Assess the morphology of the red blood cells.
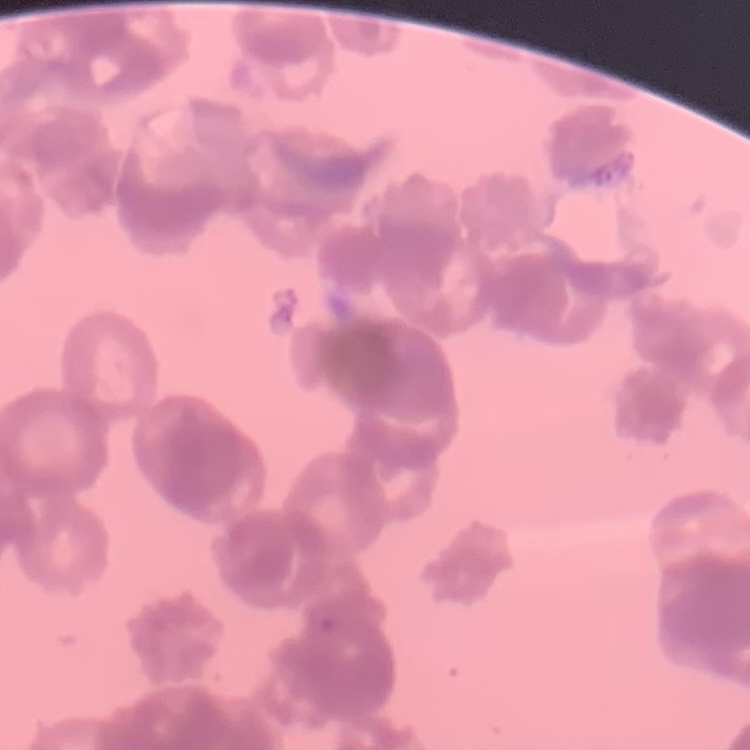

Rouleaux formation.

Field's or Giemsa stain. Square crop of a larger photomicrograph. Thin peripheral smear.